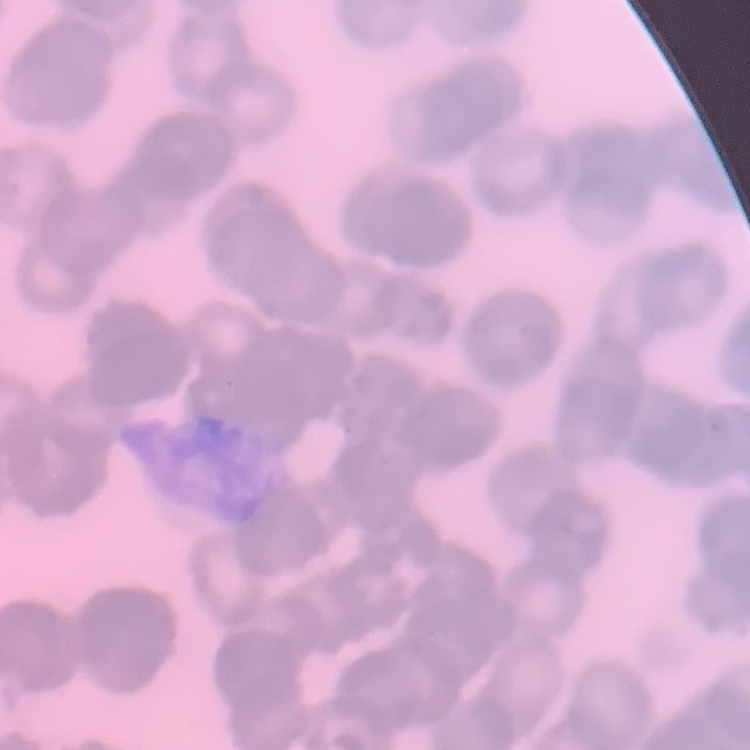

The erythrocytes exhibit rouleaux formation. One tile cut from a larger photomicrograph. Field's or Giemsa stain. Thin blood smear.